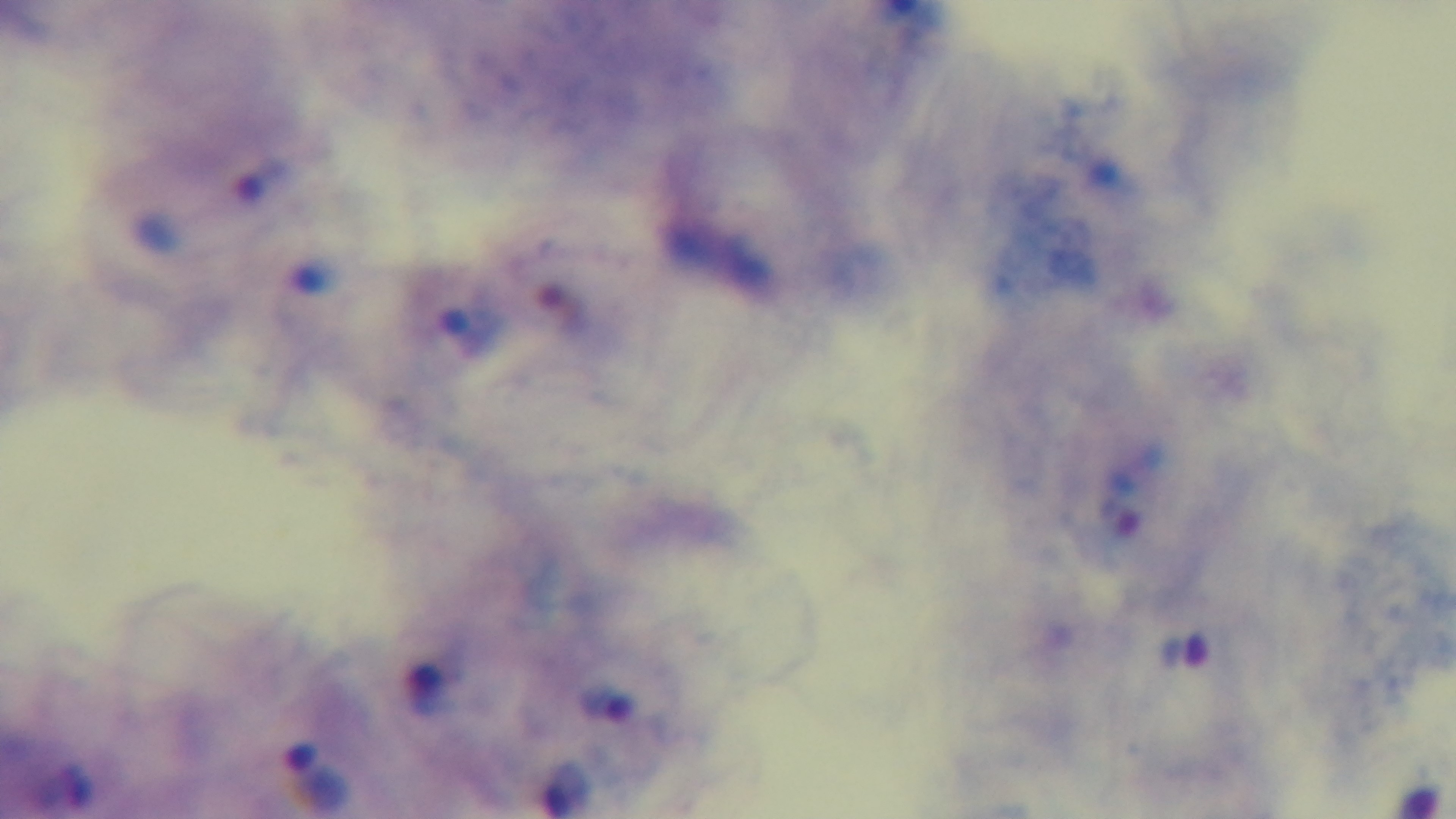
Summary:
  - Stain: Giemsa
  - Preparation: thick blood film
  - Modality: light microscopy
  - Objective: 100x oil immersion
  - Field of view: one from the slide
  - Capture: mounted 4K digital camera
  - Malaria status: positive